Locate every uninfected red blood cell.
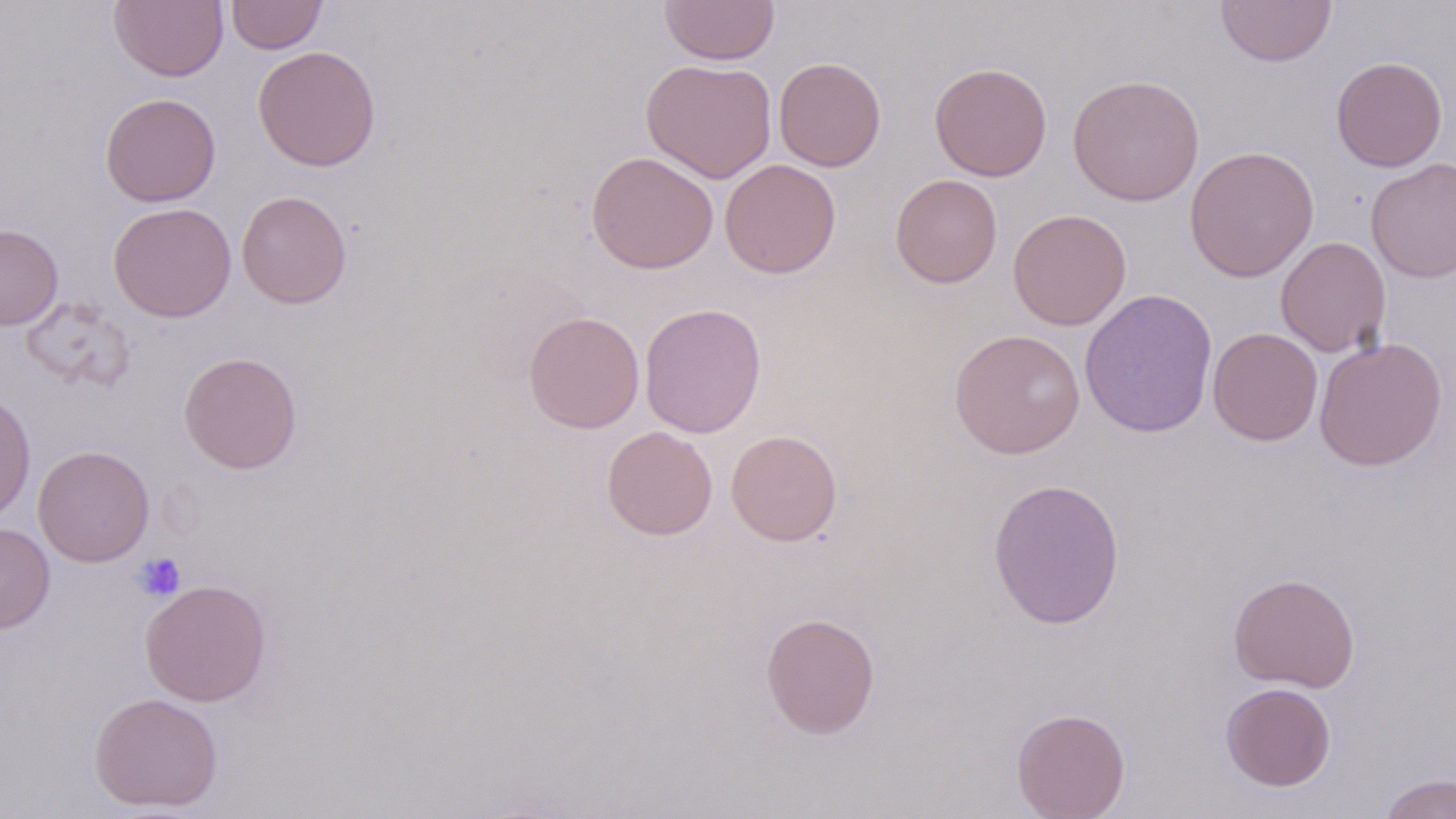
Approximate bounding boxes as (x1, y1, x2, y2) in pixels.
Uninfected red blood cells: (109, 0, 228, 82), (226, 0, 327, 54), (659, 0, 780, 66), (1215, 0, 1336, 67), (252, 45, 381, 171), (1331, 56, 1448, 172), (774, 57, 886, 172), (641, 59, 777, 183), (929, 62, 1052, 181), (1068, 74, 1204, 206), (99, 92, 221, 207), (1184, 145, 1320, 282), (586, 151, 719, 274), (1366, 158, 1456, 283), (719, 159, 841, 278), (889, 174, 1003, 288), (236, 190, 352, 309), (108, 202, 236, 322), (1007, 209, 1131, 330), (0, 223, 63, 331), (1275, 236, 1391, 358), (1079, 288, 1218, 438), (19, 297, 136, 392), (639, 302, 767, 438), (523, 311, 644, 433), (1207, 326, 1323, 446), (949, 328, 1086, 459), (1314, 336, 1447, 471), (178, 351, 303, 474), (0, 391, 36, 525), (601, 425, 718, 540), (726, 429, 842, 546), (33, 445, 155, 567), (987, 477, 1126, 630), (0, 521, 55, 633), (1228, 572, 1360, 692), (139, 579, 272, 707), (760, 611, 880, 739), (1220, 682, 1336, 791), (88, 691, 224, 813), (1011, 708, 1130, 818), (1378, 773, 1455, 819).

Platelet locations: (134, 552, 186, 601). Slide-level diagnosis: no evidence of blood parasites. One field of a larger specimen. Image is 1456×819 pixels. 1000x magnification. Thin blood smear. Light microscopy. May-Grünwald-Giemsa-stained preparation.